Describe the morphology of the erythrocytes.
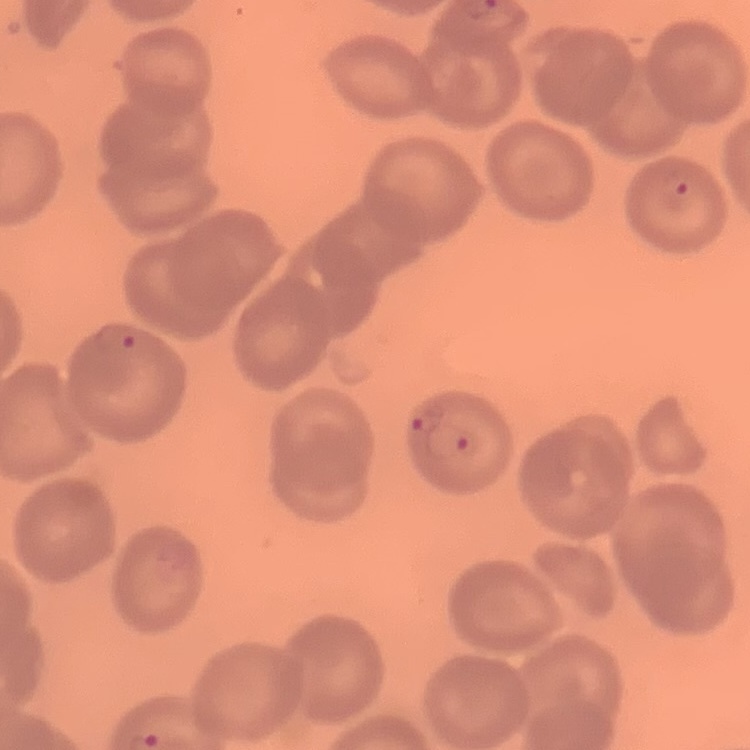
No rouleaux formation.

preparation = thin peripheral smear
stain = Field's or Giemsa
image type = square crop of a larger photomicrograph